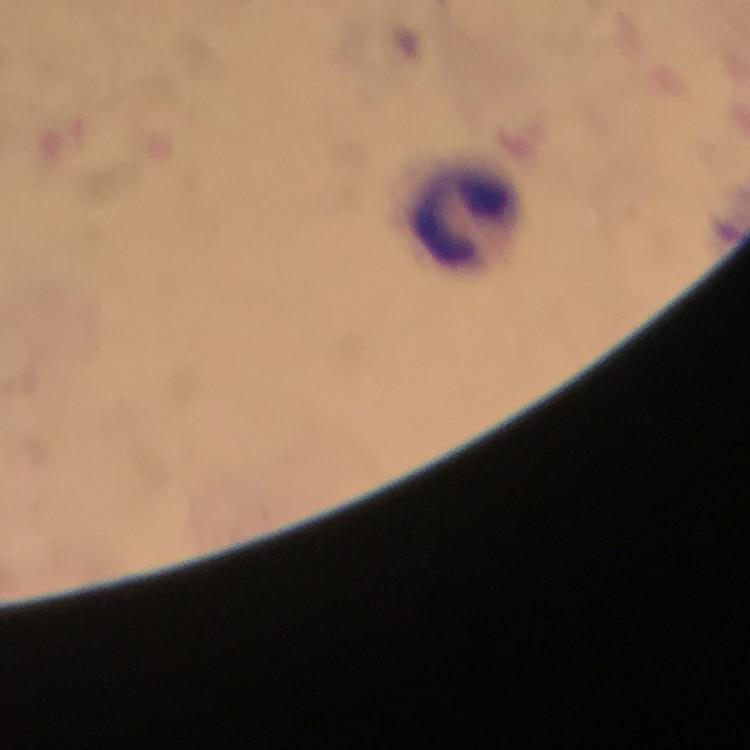
Approximate object centers, in pixels from the top-left corner.
Summary:
  - Leukocyte locations: (x=468, y=216)
  - Image size: 750×750 pixels
  - Malaria parasites: none detected
  - Cropped from: one field of view
  - Stain: Giemsa
  - Preparation: thick blood smear
  - Context: from a malaria diagnostic workup
  - Magnification: 100x
  - Immersion oil: used
  - Capture: smartphone photograph through a microscope